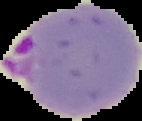
Image is 142×121 pixels. From a thin blood film. Segmented cell region on a black background. Malaria status: parasitized.